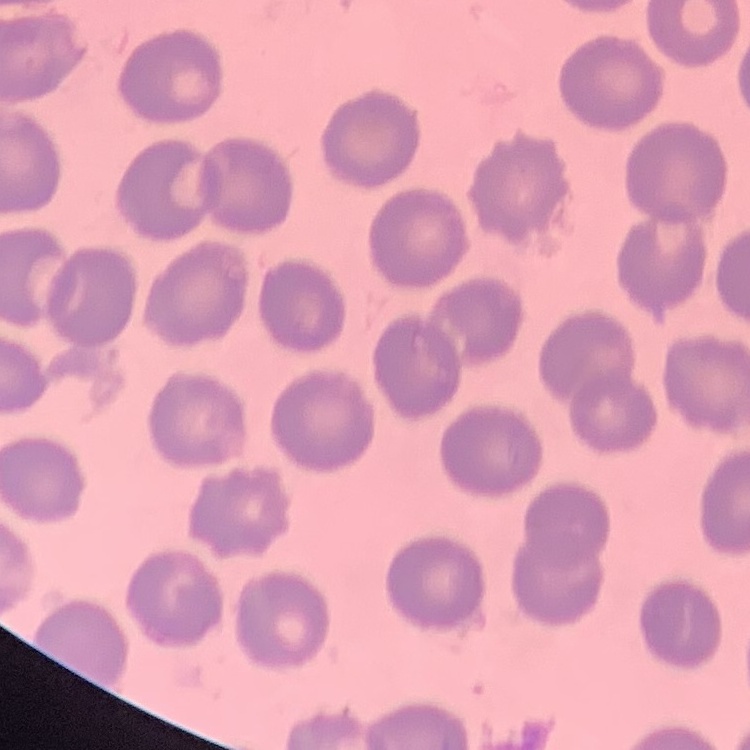
red blood cell morphology = no rouleaux formation
stain = Field's or Giemsa
preparation = thin peripheral smear
image type = one tile cut from a larger photomicrograph